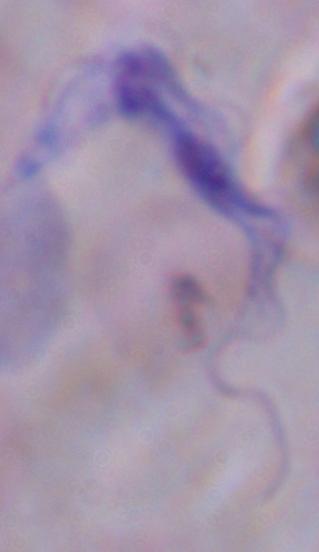
Captured at 1000x magnification. Photomicrograph. A trypanosome is seen.